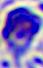

Summary:
  - Identification: leukocyte
  - Magnification: 400x
  - Modality: photomicrograph